Identify the parasite.
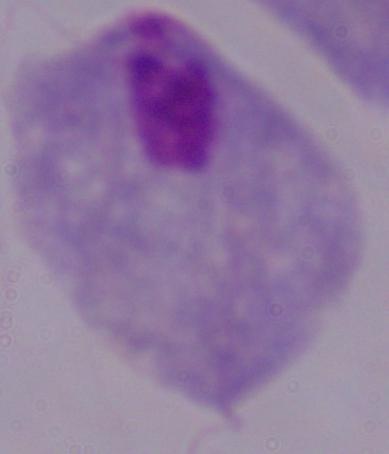

A trichomonad.

Summary:
  - Magnification: 1000x
  - Modality: photomicrograph